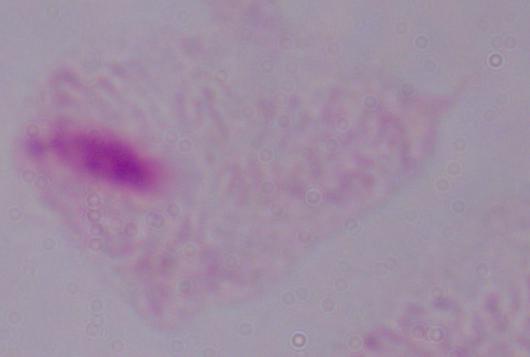

Summary:
  - Magnification: 1000x
  - Identification: trichomonad
  - Modality: photomicrograph